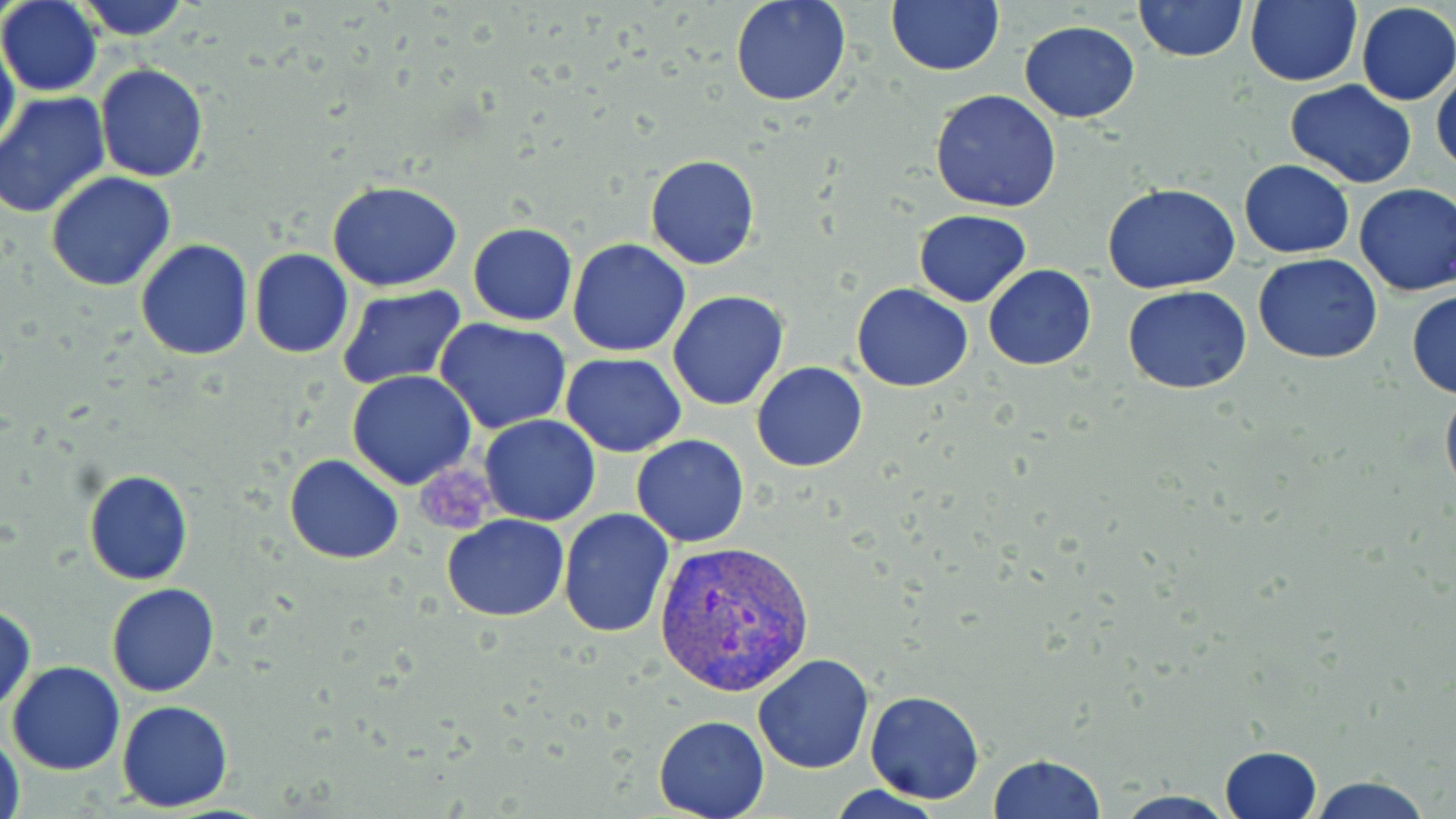

slide-level diagnosis = Plasmodium vivax
image size = 1456×819 pixels
preparation = thin blood film
magnification = 1000x
stain = May-Grünwald-Giemsa
field of view = one of a larger specimen
platelet locations = approximate bounding boxes as (x1, y1, x2, y2) in pixels: (416, 456, 504, 536)
uninfected red blood cell locations = approximate bounding boxes as (x1, y1, x2, y2) in pixels: (70, 0, 192, 41), (729, 0, 852, 107), (885, 0, 1002, 75), (1133, 0, 1248, 64), (1245, 0, 1361, 86), (0, 1, 103, 96), (1355, 3, 1455, 106), (1018, 20, 1142, 124), (0, 34, 19, 162), (1432, 61, 1456, 177), (94, 64, 208, 183), (1, 79, 206, 202), (1285, 80, 1418, 188), (930, 89, 1062, 212), (0, 92, 110, 218), (645, 154, 760, 270), (1238, 158, 1354, 259), (46, 171, 178, 292), (328, 180, 463, 292), (1103, 183, 1241, 294), (1354, 183, 1456, 298), (914, 210, 1031, 307), (468, 223, 577, 326), (567, 238, 691, 356), (135, 239, 252, 359), (249, 249, 354, 360), (1253, 253, 1383, 363), (984, 264, 1096, 372), (851, 281, 973, 393), (1123, 285, 1251, 395), (338, 286, 467, 388), (1407, 289, 1456, 399), (666, 290, 790, 411), (433, 319, 573, 435), (362, 333, 534, 469), (563, 353, 686, 456), (751, 361, 868, 473), (347, 371, 477, 490), (1440, 382, 1456, 507), (479, 414, 601, 526), (631, 435, 749, 546), (285, 454, 403, 565), (83, 469, 193, 586), (557, 508, 674, 639), (442, 515, 570, 621), (106, 583, 221, 697), (1, 599, 35, 714), (752, 654, 875, 773), (7, 660, 126, 774), (864, 690, 983, 804), (117, 700, 233, 811), (653, 715, 771, 819), (2, 732, 25, 819), (1217, 746, 1323, 819), (988, 754, 1107, 818), (1302, 773, 1436, 819), (824, 785, 948, 818), (1107, 791, 1243, 819)
Plasmodium vivax-infected red blood cell locations = approximate bounding boxes as (x1, y1, x2, y2) in pixels: (652, 537, 816, 696)
modality = optical microscopy